State which parasite is depicted.
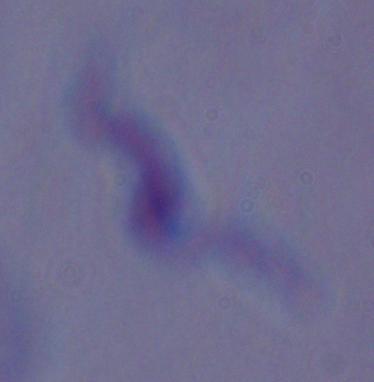

A trypanosome.

{
  "modality": "photomicrograph",
  "magnification": "1000x"
}